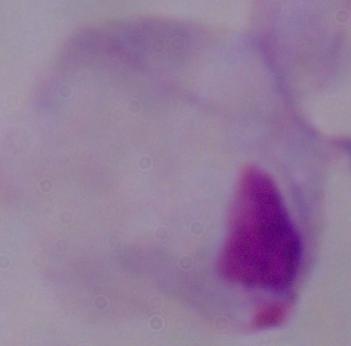

modality = micrograph
identification = trichomonad
magnification = 1000x